Identify the preparation type.
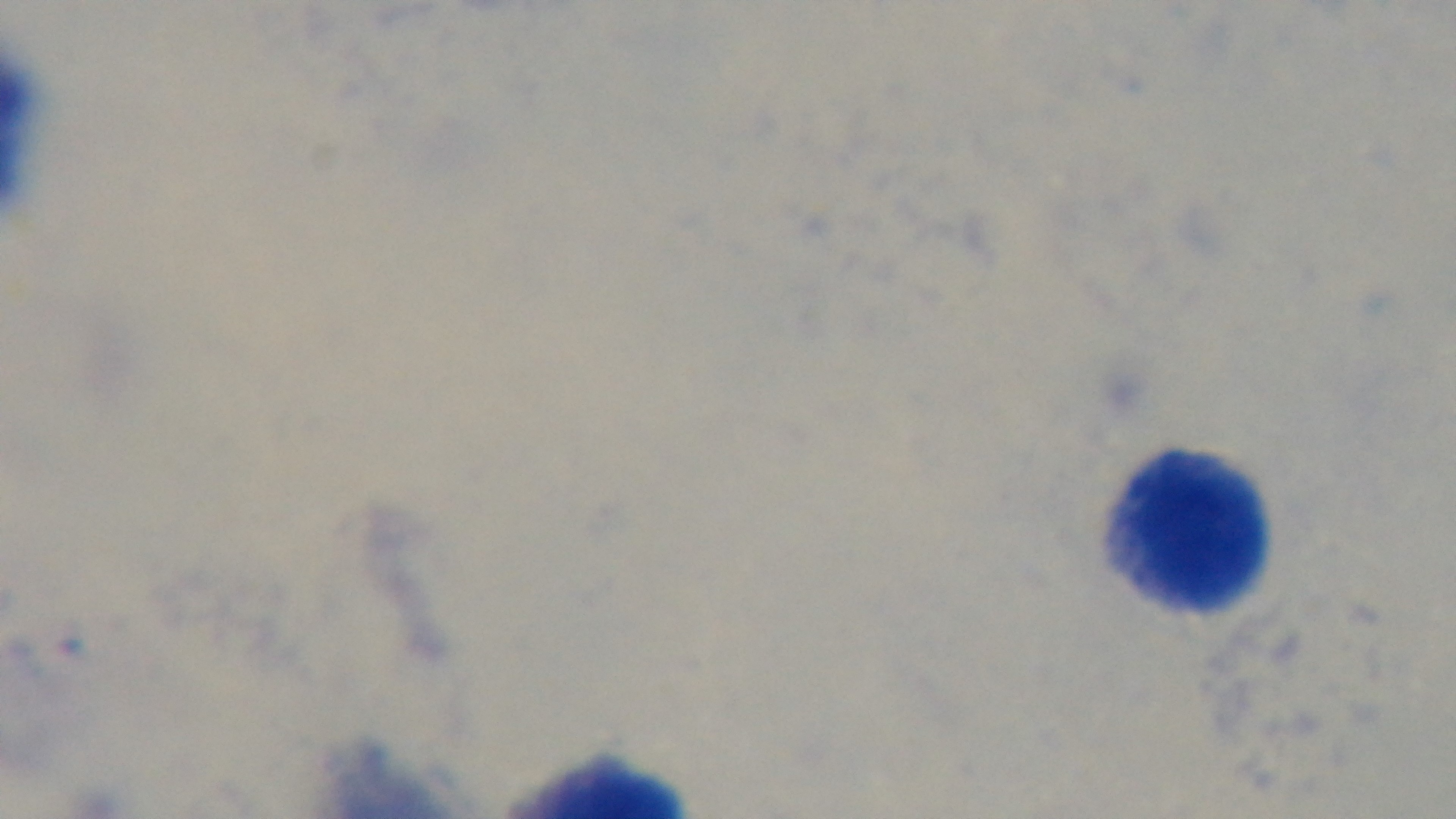

It is a thick blood film.

{
  "field_of_view": "single",
  "objective": "100x oil immersion",
  "stain": "Giemsa",
  "capture": "mounted 4K digital camera",
  "malaria_status": "uninfected",
  "modality": "light microscopy"
}